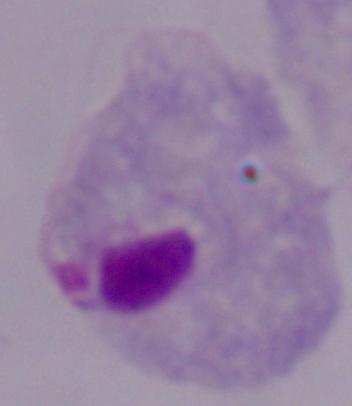

Micrograph. A trichomonad is seen. 1000x magnification.